Locate malaria parasites and leukocytes.
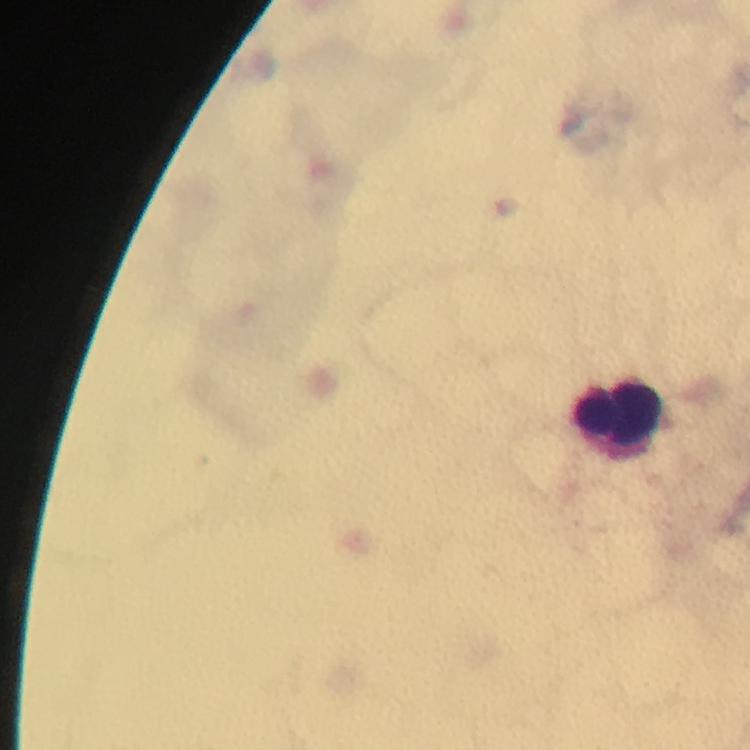
No malaria parasites detected.
Approximate centers as {x, y} in pixels.
Leukocytes: {623, 418}.

A crop from one field of view. Photographed through the microscope with a smartphone camera. Image is 750×750 pixels. Thick smear. From a diagnostic examination for malaria. Immersion oil was used. Giemsa stain. At 100x magnification.